Classify the preparation.
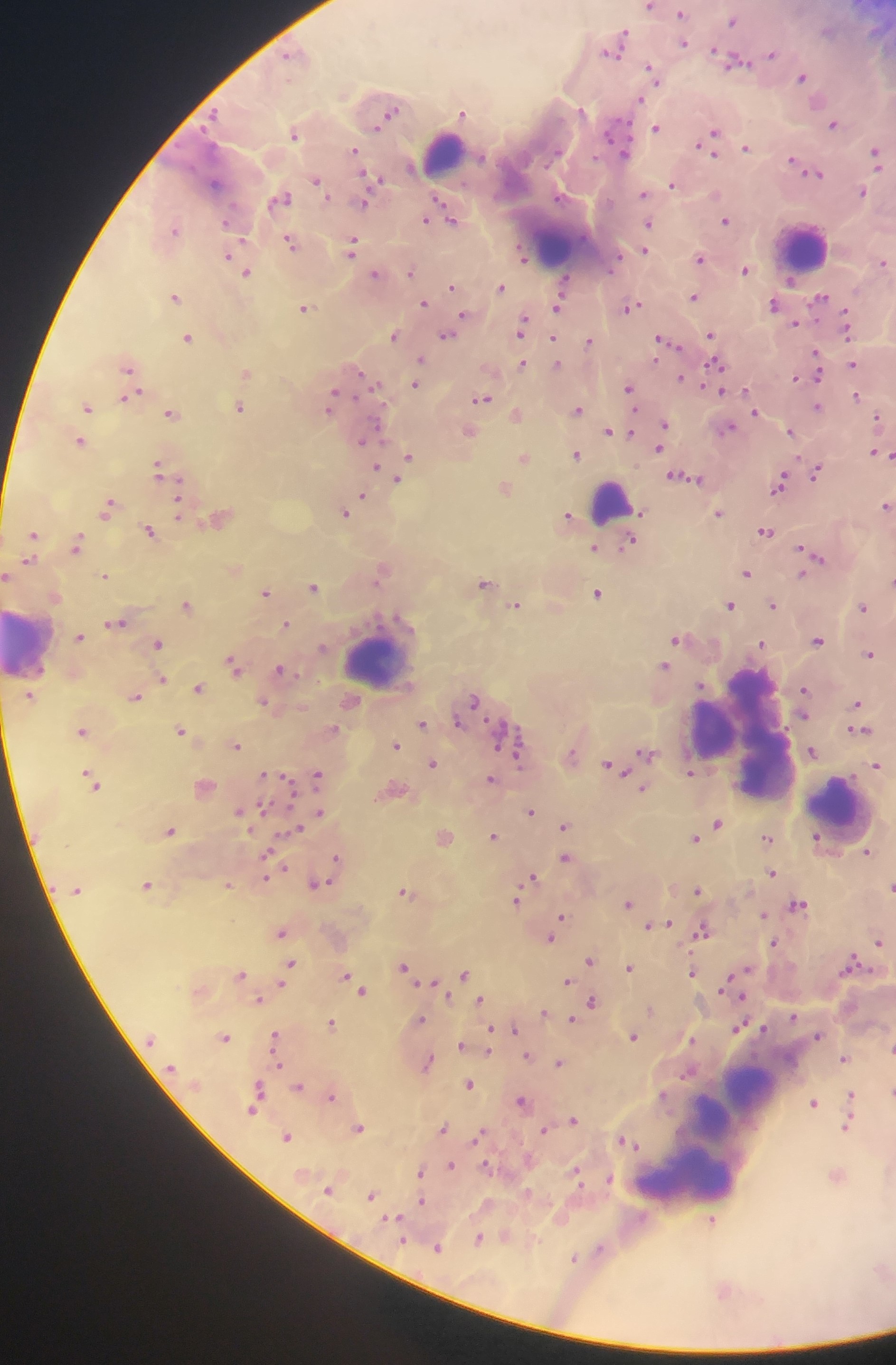
This is a thick smear.

Approximate centers as (x, y) in pixels.
Summary:
  - Leukocyte locations: (441, 156), (555, 246), (806, 249), (614, 503), (26, 646), (376, 658), (744, 733), (838, 804), (750, 1079), (715, 1120), (689, 1177)
  - Malaria parasite locations: (649, 7), (682, 14), (733, 21), (623, 35), (683, 43), (615, 47), (772, 53), (737, 61), (652, 71), (803, 77), (639, 99), (583, 111), (392, 112), (464, 113), (833, 124), (615, 127), (656, 127), (294, 133), (713, 133), (746, 147), (354, 151), (876, 153), (625, 154), (792, 162), (411, 167), (815, 173), (372, 178), (317, 181), (215, 184), (673, 185), (863, 192), (644, 194), (559, 197), (281, 199), (365, 204), (425, 220), (454, 220), (726, 220), (649, 224), (174, 229), (290, 243), (353, 247), (645, 250), (230, 253), (523, 256), (700, 258), (882, 262), (745, 270), (412, 271), (247, 273), (375, 273), (791, 281), (452, 286), (500, 287), (175, 297), (694, 297), (820, 299), (423, 303), (774, 305), (558, 306), (631, 306), (304, 308), (463, 315), (796, 323), (522, 326), (847, 329), (448, 334), (395, 335), (711, 335), (188, 338), (590, 341), (663, 341), (816, 354), (421, 361), (522, 363), (557, 363), (853, 364), (716, 365), (127, 366), (246, 372), (419, 372), (360, 373), (817, 374), (796, 376), (681, 378), (416, 384), (629, 388), (130, 396), (857, 397), (482, 398), (331, 401), (88, 407), (816, 407), (241, 408), (577, 410), (754, 412), (171, 414), (516, 415), (879, 419), (664, 425), (728, 427), (610, 431), (791, 431), (372, 433), (470, 433), (80, 441), (660, 446), (874, 452), (576, 454), (890, 456), (410, 457), (524, 458), (158, 467), (376, 467), (816, 471), (680, 477), (401, 479), (779, 484), (504, 488), (180, 494), (362, 498), (108, 505), (179, 506), (886, 506), (346, 511), (719, 513), (567, 516), (219, 519), (149, 531), (765, 532), (34, 535), (630, 541), (78, 543), (594, 548), (805, 551), (814, 555), (29, 561), (382, 572), (746, 572), (106, 574), (800, 575), (6, 576), (485, 584), (314, 587), (266, 592), (598, 593), (187, 604), (729, 604), (772, 604), (515, 605), (863, 606), (116, 622), (286, 623), (80, 637), (676, 639), (817, 639), (761, 643), (158, 644), (869, 654), (233, 665), (664, 666), (281, 670), (163, 679), (700, 684), (199, 688), (804, 690), (30, 696), (135, 697), (473, 699), (264, 702), (857, 703), (803, 716), (458, 722), (422, 723), (82, 730), (861, 730), (181, 731), (513, 738), (236, 745), (396, 745), (812, 751), (519, 752), (647, 753), (433, 763), (611, 765), (877, 765), (690, 769), (318, 775), (91, 778), (490, 779), (644, 789), (242, 810), (531, 811), (318, 814), (717, 823), (565, 825), (296, 829), (170, 830), (445, 836), (493, 836), (816, 837), (694, 838), (767, 838), (868, 853), (565, 858), (336, 859), (270, 872), (771, 873), (532, 877), (147, 885), (228, 885), (317, 885), (891, 888), (697, 890), (405, 892), (516, 900), (628, 903), (798, 905), (763, 914), (560, 916), (663, 924), (652, 926), (557, 927), (703, 930), (280, 932), (551, 939), (878, 940), (774, 943), (591, 960), (851, 963), (291, 964), (404, 966), (629, 968), (745, 972), (241, 973), (692, 973), (465, 975), (346, 977), (566, 981), (354, 983), (361, 990), (259, 1000), (481, 1001), (592, 1001), (544, 1012), (794, 1017), (420, 1019), (572, 1021), (331, 1024), (739, 1027), (516, 1030), (490, 1032), (275, 1035), (818, 1035), (225, 1037), (634, 1037), (460, 1044), (488, 1052), (527, 1056), (845, 1058), (428, 1063), (559, 1063), (279, 1065), (469, 1083), (299, 1086), (259, 1092), (851, 1095), (331, 1096), (521, 1100), (814, 1103), (253, 1110), (574, 1119), (847, 1127), (443, 1128), (359, 1129), (543, 1130), (480, 1133), (286, 1137), (624, 1142), (450, 1166), (485, 1166), (420, 1172), (576, 1174), (609, 1179), (329, 1190), (371, 1195), (422, 1201), (395, 1218), (712, 1221), (478, 1239), (403, 1240), (438, 1247), (600, 1249), (573, 1259)
  - Field of view: single
  - Capture: mobile-phone photograph through a microscope
  - Image size: 896×1365 pixels
  - Country: Ghana